Comment on the morphology of the red blood cells.
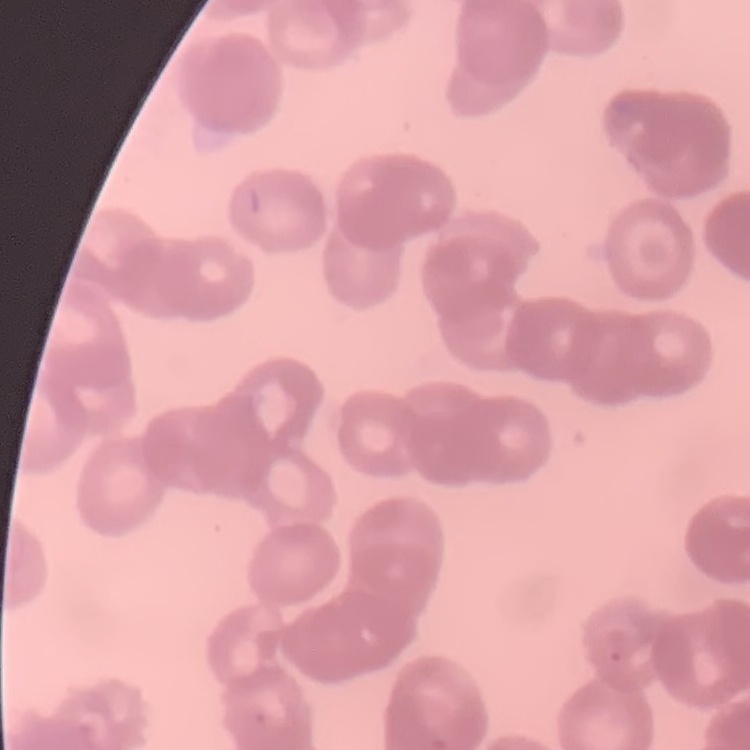
Rouleaux formation.

stain = Field's or Giemsa
preparation = thin peripheral smear
image type = square crop of a larger photomicrograph